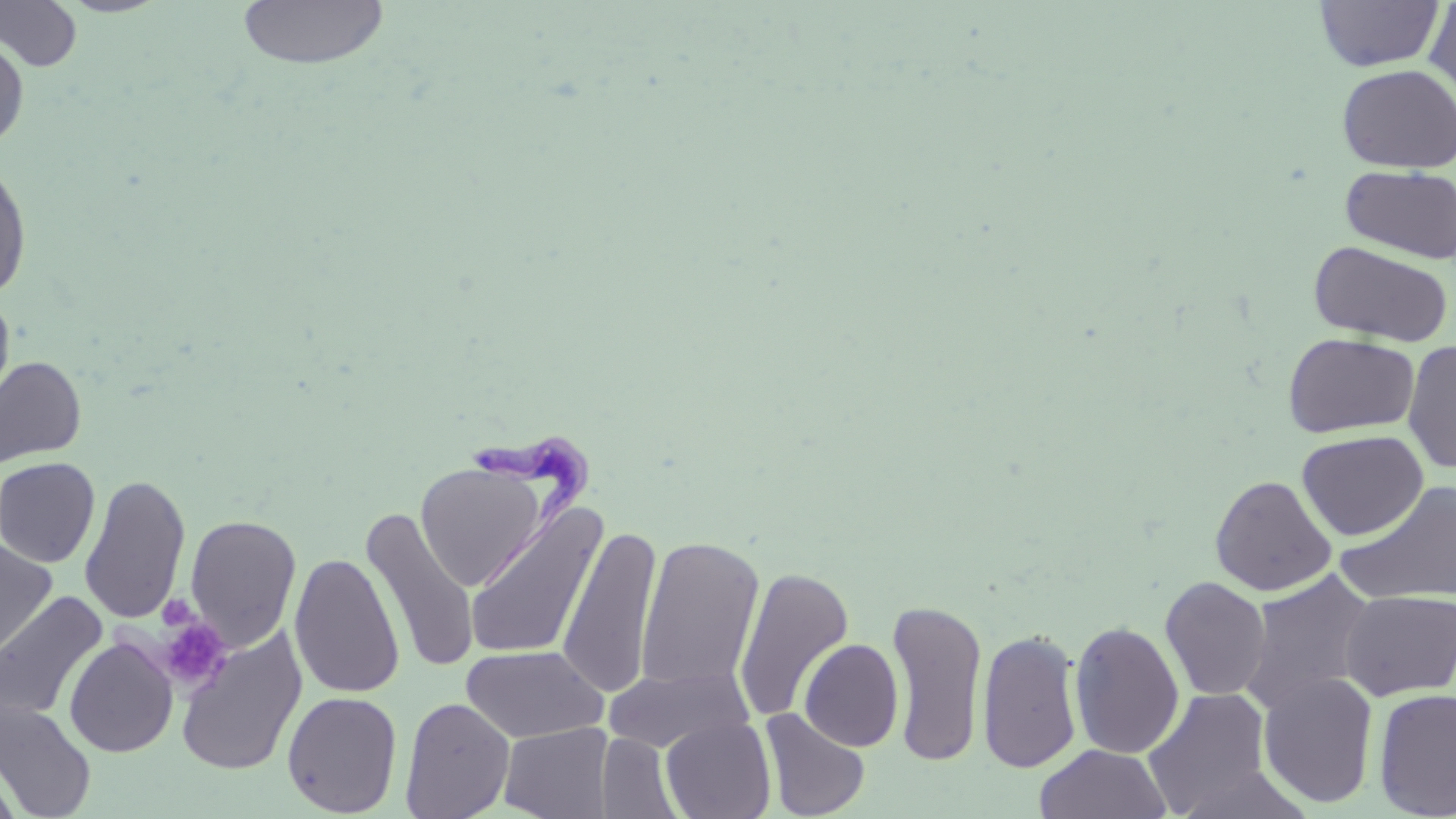
Summary:
  - Coordinate format: approximate bounding boxes as (x1, y1, x2, y2) in pixels
  - Platelet locations: (157, 595, 200, 632), (158, 617, 231, 692)
  - Uninfected red blood cell locations: (0, 1, 83, 73), (236, 1, 390, 71), (1313, 1, 1445, 71), (1423, 2, 1456, 106), (0, 33, 30, 152), (1336, 64, 1456, 173), (0, 159, 33, 302), (1340, 165, 1456, 264), (1308, 240, 1453, 348), (0, 288, 15, 414), (1282, 332, 1420, 438), (1402, 340, 1456, 474), (0, 356, 87, 470), (1297, 430, 1428, 540), (0, 457, 100, 568), (415, 460, 549, 591), (79, 474, 191, 625), (1210, 475, 1336, 596), (1335, 481, 1456, 605), (464, 501, 608, 663), (361, 506, 480, 675), (184, 514, 302, 652), (558, 524, 662, 698), (636, 535, 765, 694), (0, 538, 58, 659), (289, 552, 405, 699), (733, 566, 854, 724), (1239, 569, 1379, 715), (1160, 576, 1271, 701), (1340, 589, 1456, 700), (0, 591, 109, 726), (886, 597, 988, 767), (1069, 620, 1184, 759), (175, 627, 307, 777), (977, 628, 1083, 774), (64, 636, 178, 758), (799, 638, 904, 752), (461, 644, 608, 742), (602, 664, 753, 754), (1257, 672, 1379, 808), (1373, 687, 1456, 818), (1142, 688, 1273, 817), (282, 691, 402, 817), (399, 697, 516, 819), (1, 700, 96, 818), (760, 707, 871, 819), (660, 714, 776, 819), (499, 722, 614, 819), (597, 733, 682, 818), (1034, 744, 1172, 819), (0, 757, 25, 819)
  - Trypanosoma brucei locations: (465, 426, 604, 594)
  - Slide-level diagnosis: Trypanosoma brucei
  - Field of view: one of a larger specimen
  - Stain: May-Grünwald-Giemsa
  - Modality: light microscopy
  - Magnification: 1000x
  - Preparation: thin blood smear
  - Image size: 1456×819 pixels